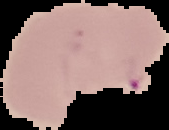
The area outside the segmented cell region is set to black. Image is 169×130 pixels. Result: malaria parasites detected. From a thin blood film.